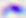
Summary:
  - Magnification: 400x
  - Identification: Toxoplasma gondii
  - Modality: photomicrograph